Name the parasite shown.
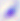

Toxoplasma gondii.

{
  "magnification": "400x",
  "modality": "photomicrograph"
}